Classify this cell by malaria status.
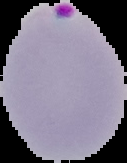

It is parasitized.

preparation = thin blood smear
image size = 127×163 pixels
image type = cell region segmented out of the field of view; surrounding area masked to black